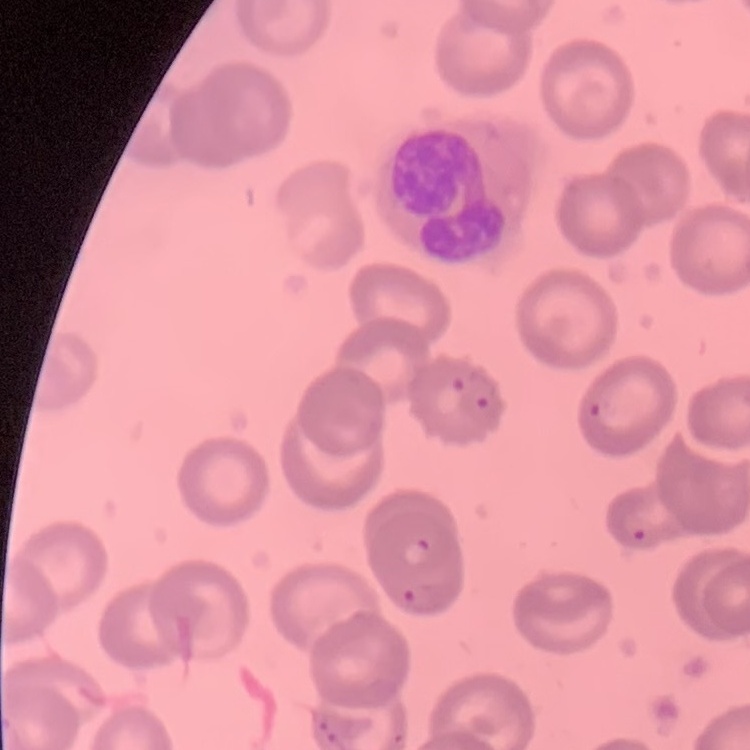

Summary:
  - Erythrocyte morphology: no rouleaux formation
  - Stain: Field's or Giemsa
  - Image type: square crop of a larger photomicrograph
  - Preparation: thin blood smear